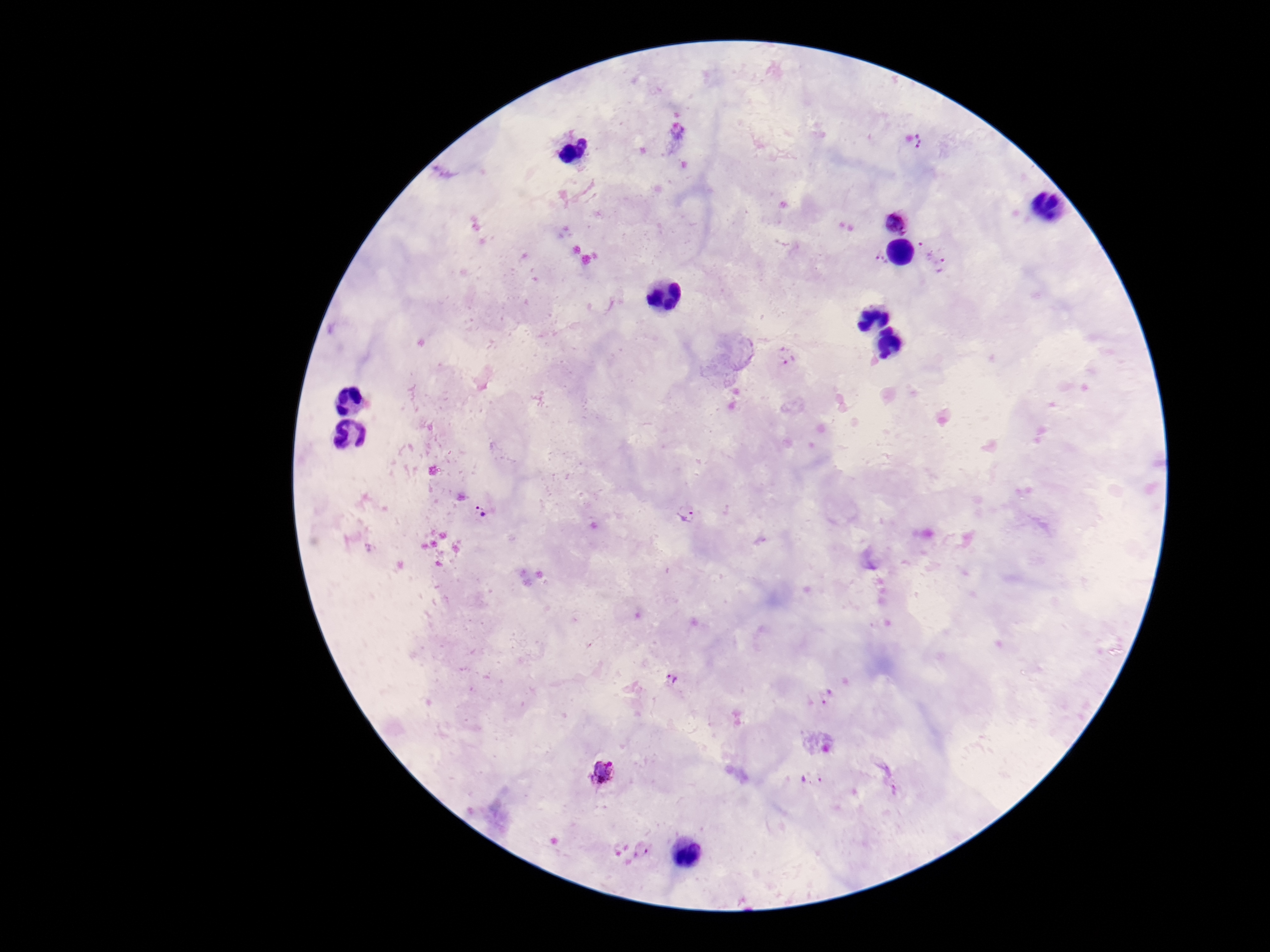
Approximate centers as (x, y) in pixels. Plasmodium parasite locations: (920, 141), (898, 221), (925, 247), (881, 260), (941, 264), (788, 356), (483, 514), (686, 514), (672, 679), (826, 696), (604, 774), (811, 780), (643, 850). 100x magnification. Thick blood smear. Giemsa stain. Photographed through the microscope eyepiece with a smartphone camera. One field from this slide. Patient malaria status: infected. Image is 1270×952 pixels.